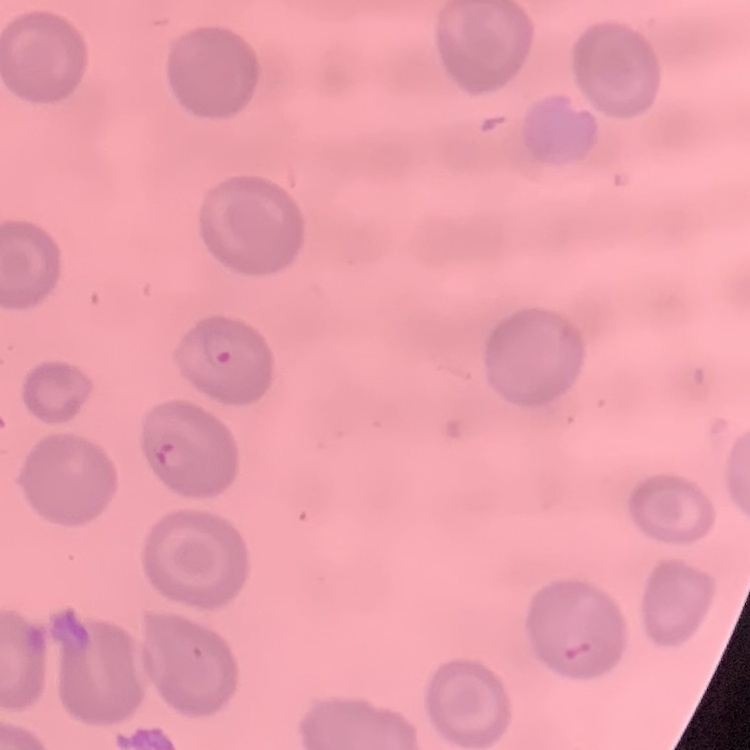
The red blood cells exhibit no rouleaux formation. Stained with either Field's or Giemsa. One tile cut from a larger photomicrograph. Thin blood film.